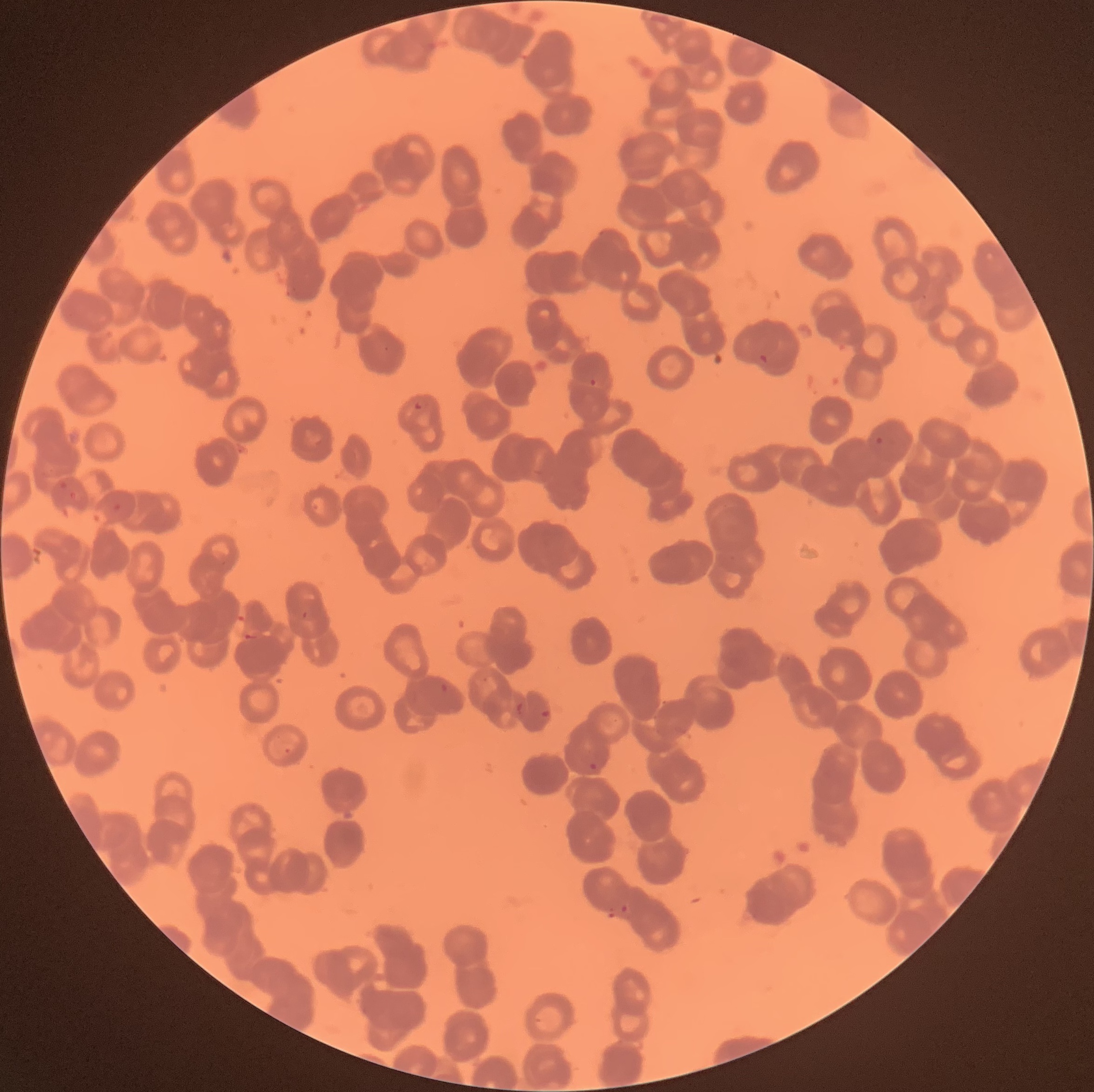

coordinate format = approximate bounding boxes as (x1, y1, x2, y2) in pixels
Plasmodium parasite locations = (757, 353, 770, 364), (589, 377, 598, 387), (412, 401, 422, 411), (875, 437, 884, 445), (439, 682, 451, 694), (540, 709, 550, 718), (588, 762, 598, 771), (619, 903, 632, 914)
image size = 1094×1092 pixels
modality = light microscopy
preparation = thin blood smear
red blood cell morphology = rouleaux formation